Assess this cell for malaria.
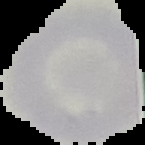

Uninfected.

Summary:
  - Preparation: thin blood smear
  - Image size: 145×145 pixels
  - Image type: segmented cell region with the area outside set to black